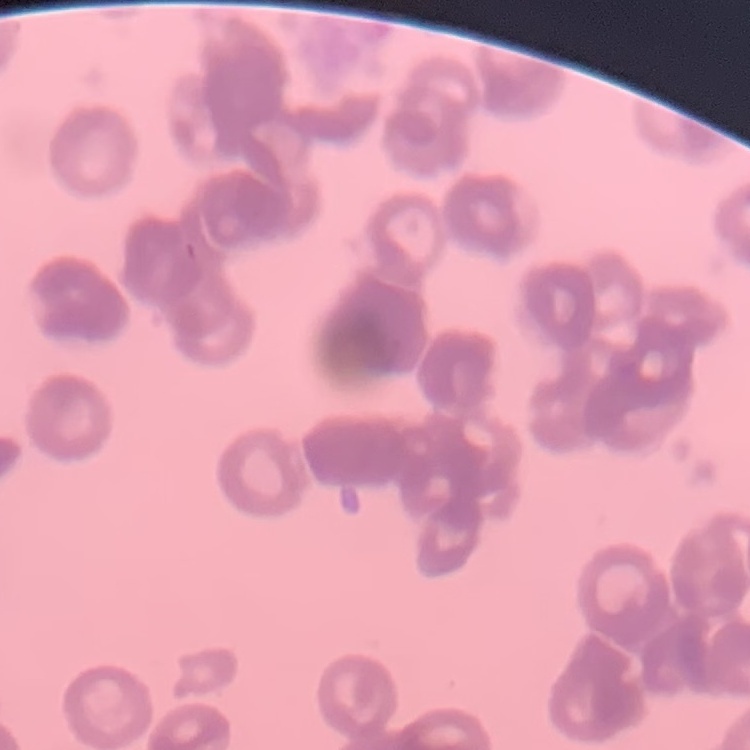

red blood cell morphology = rouleaux formation
preparation = thin peripheral smear
stain = Field's or Giemsa
image type = square crop of a larger photomicrograph